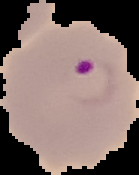
Cell region segmented out of the field of view; the surrounding area is masked to black. Result: Plasmodium parasites detected. From a thin blood smear. Image is 139×175 pixels.